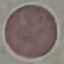

Summary:
  - Result: no malaria parasites seen
  - Image type: cell patch, automatically extracted from a larger field of view and resized to 64 × 64 pixels
  - Stain: Giemsa
  - Capture: smartphone through the microscope eyepiece
  - Preparation: thin smear